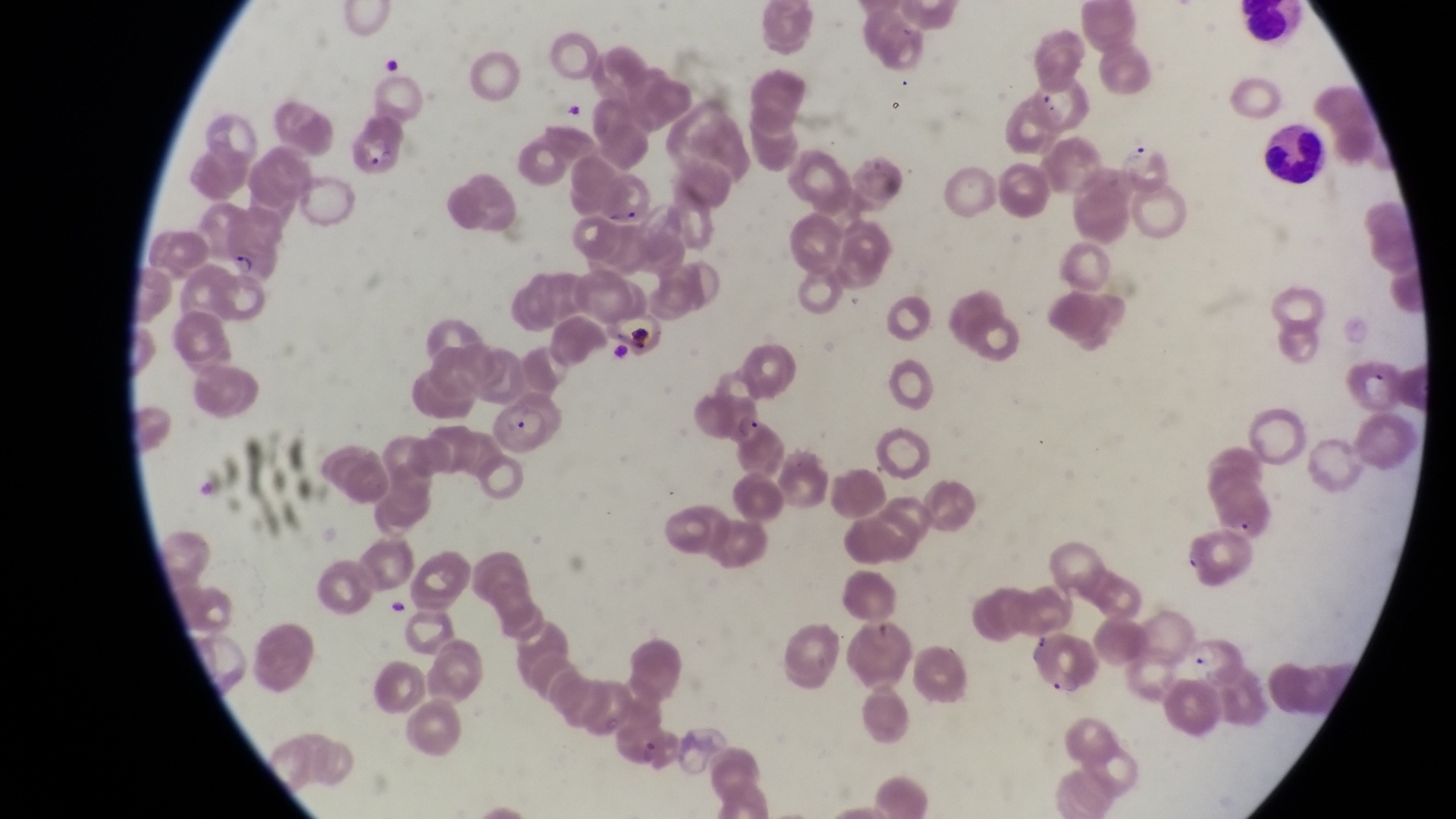
Approximate bounding boxes as {left, top, right, bottom} in pixels. Parasitised red blood cell locations: {344, 115, 405, 178}, {215, 231, 279, 283}, {1337, 351, 1401, 414}, {495, 394, 564, 458}, {1188, 620, 1244, 689}. Trophozoite locations: {733, 413, 760, 445}, {1234, 512, 1262, 543}. Artifact (platelet-like body, stain precipitate, or debris) locations: {627, 314, 654, 360}. Leukocyte locations: {1241, 5, 1312, 49}, {1266, 118, 1324, 181}. Collected in Uganda. Magnification of 1000x. One field of view. Thin blood smear. Image is 1456×819 pixels. Captured by a smartphone held over the eyepiece of an Olympus CX-23 microscope.